Report the malaria status of this cell.
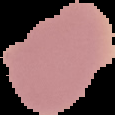

It is uninfected.

image size = 115×115 pixels
preparation = thin blood smear
image type = segmented cell region with the area outside set to black